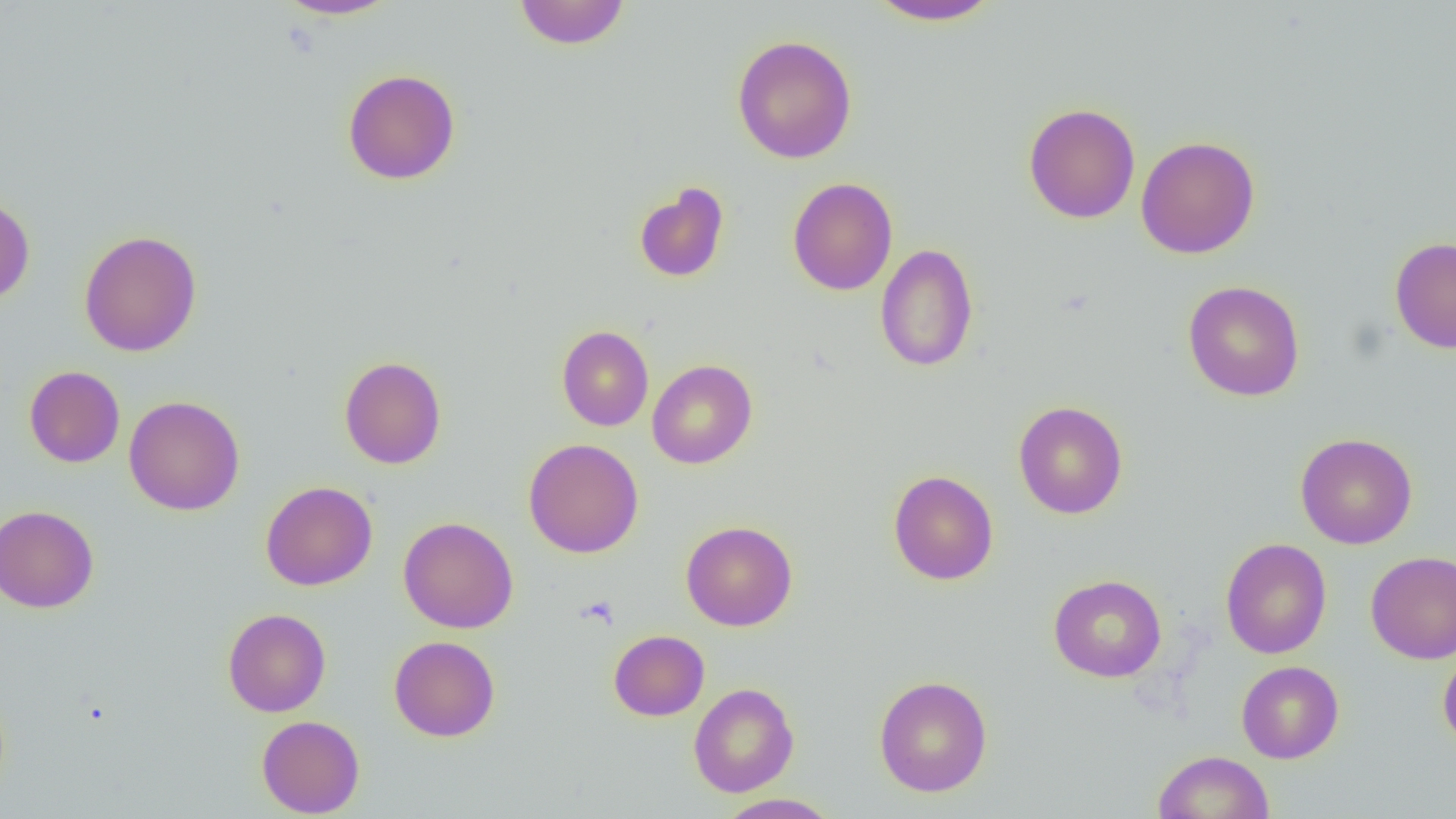

Approximate bounding boxes as [x1, y1, x2, y2] in pixels. Uninfected red blood cell locations: [275, 0, 399, 20], [865, 0, 1004, 26], [513, 1, 630, 50], [732, 34, 857, 164], [342, 68, 461, 185], [1023, 102, 1141, 224], [1135, 136, 1260, 259], [787, 177, 898, 296], [633, 181, 730, 283], [0, 194, 35, 305], [78, 230, 202, 356], [1390, 236, 1456, 353], [875, 243, 979, 373], [1183, 280, 1305, 401], [557, 325, 654, 431], [339, 356, 447, 469], [647, 359, 758, 469], [24, 366, 125, 467], [124, 395, 245, 516], [1013, 400, 1128, 519], [1295, 432, 1418, 550], [523, 438, 644, 559], [888, 469, 999, 585], [260, 481, 377, 591], [0, 505, 99, 613], [398, 516, 518, 633], [680, 520, 798, 631], [1220, 538, 1331, 659], [1366, 550, 1456, 663], [1049, 574, 1166, 682], [222, 608, 331, 717], [608, 630, 709, 720], [389, 636, 500, 741], [1438, 645, 1456, 753], [1236, 660, 1344, 764], [874, 675, 992, 797], [688, 683, 799, 797], [256, 715, 365, 818], [1153, 750, 1275, 819], [715, 793, 842, 819]. Slide-level diagnosis: no evidence of blood parasites. Image is 1456×819 pixels. Optical microscopy. 1000x magnification. Single field of view. Thin blood smear.